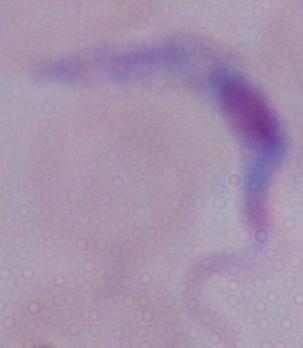
A trypanosome is shown. Captured at 1000x magnification. Micrograph.